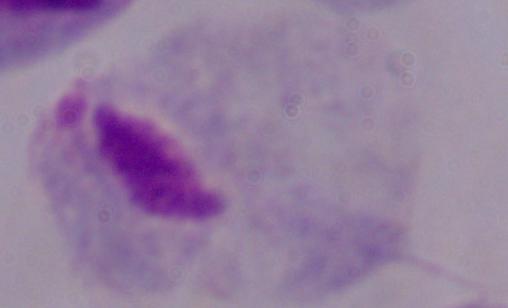
1000x magnification. A trichomonad is shown. Photomicrograph.